Report the malaria status of this cell.
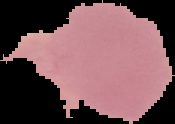
Uninfected.

Summary:
  - Preparation: thin blood smear
  - Image size: 175×124 pixels
  - Image type: segmented cell region on a black background